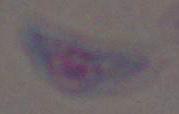
identification = Toxoplasma gondii
magnification = 1000x
modality = photomicrograph